Find the cells and give the type of each one.
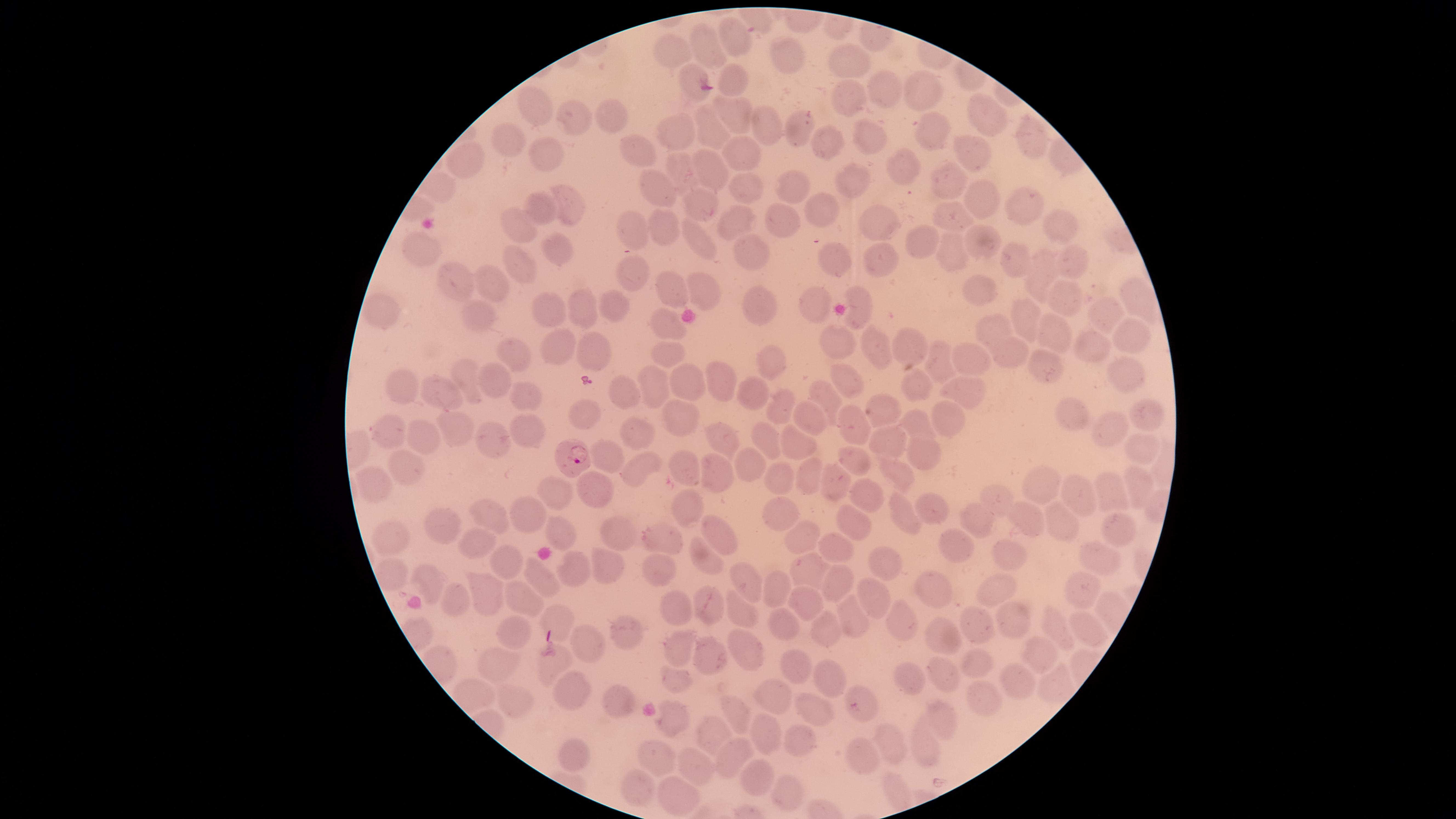
Approximate marker points as {x, y} in pixels.
Parasitized red blood cells: {575, 459}.
Uninfected red blood cells: {737, 39}, {708, 46}, {669, 52}, {783, 60}, {849, 62}, {883, 89}, {845, 95}, {918, 95}, {538, 103}, {609, 115}, {735, 116}, {983, 117}, {577, 118}, {762, 124}, {934, 127}, {795, 129}, {711, 132}, {679, 134}, {867, 137}, {828, 139}, {509, 140}, {1034, 141}, {542, 149}, {639, 151}, {967, 153}, {742, 155}, {466, 157}, {903, 164}, {712, 170}, {680, 171}, {851, 179}, {948, 183}, {793, 187}, {745, 190}, {657, 194}, {980, 196}, {567, 199}, {697, 206}, {1025, 206}, {825, 210}, {544, 211}, {951, 216}, {737, 218}, {783, 219}, {884, 220}, {633, 224}, {516, 226}, {1056, 226}, {669, 229}, {921, 237}, {701, 241}, {981, 243}, {419, 248}, {753, 250}, {954, 252}, {557, 253}, {832, 256}, {879, 259}, {1069, 259}, {1015, 260}, {518, 264}, {632, 271}, {1039, 275}, {454, 280}, {493, 282}, {665, 287}, {704, 293}, {982, 293}, {1135, 294}, {1062, 296}, {861, 301}, {615, 306}, {811, 306}, {579, 307}, {756, 308}, {1103, 310}, {385, 311}, {551, 311}, {477, 315}, {1025, 317}, {662, 324}, {992, 329}, {1049, 334}, {1131, 338}, {910, 342}, {874, 343}, {1100, 343}, {837, 344}, {560, 345}, {512, 351}, {592, 351}, {662, 352}, {1003, 352}, {940, 357}, {970, 360}, {769, 361}, {1046, 362}, {1124, 372}, {462, 375}, {723, 379}, {408, 380}, {500, 381}, {689, 383}, {656, 384}, {846, 386}, {918, 388}, {965, 391}, {758, 393}, {442, 394}, {619, 394}, {822, 394}, {521, 395}, {784, 400}, {577, 411}, {1067, 412}, {677, 413}, {815, 415}, {1145, 415}, {884, 416}, {942, 416}, {845, 419}, {917, 423}, {450, 424}, {385, 425}, {529, 425}, {633, 433}, {720, 433}, {1112, 434}, {768, 436}, {424, 437}, {493, 438}, {889, 439}, {794, 444}, {926, 447}, {1140, 447}, {609, 452}, {856, 458}, {750, 461}, {678, 462}, {638, 464}, {407, 469}, {720, 469}, {898, 473}, {807, 476}, {777, 478}, {837, 480}, {1135, 482}, {372, 484}, {596, 486}, {1043, 486}, {559, 492}, {1111, 493}, {994, 494}, {867, 496}, {1075, 498}, {686, 500}, {527, 504}, {933, 509}, {781, 512}, {495, 514}, {1026, 516}, {908, 517}, {984, 519}, {1058, 520}, {442, 521}, {849, 521}, {1116, 525}, {616, 526}, {712, 533}, {560, 535}, {653, 535}, {805, 536}, {479, 540}, {391, 544}, {835, 548}, {954, 548}, {1003, 552}, {709, 558}, {1104, 558}, {504, 559}, {888, 562}, {600, 564}, {569, 568}, {811, 569}, {658, 571}, {391, 575}, {431, 578}, {745, 580}, {542, 581}, {835, 583}, {775, 589}, {991, 590}, {488, 591}, {929, 591}, {1081, 592}, {873, 595}, {516, 598}, {459, 603}, {802, 604}, {671, 605}, {698, 605}, {557, 614}, {735, 614}, {853, 620}, {900, 620}, {975, 620}, {1020, 621}, {1079, 625}, {789, 626}, {1058, 628}, {826, 631}, {626, 632}, {519, 634}, {936, 634}, {584, 644}, {678, 645}, {746, 651}, {712, 652}, {1036, 653}, {495, 660}, {977, 663}, {551, 666}, {797, 669}, {944, 674}, {676, 680}, {823, 680}, {913, 680}, {1023, 682}, {571, 684}, {619, 695}, {979, 697}, {769, 698}, {513, 699}, {735, 705}, {863, 707}, {812, 709}, {940, 713}, {677, 718}, {713, 726}, {767, 729}, {794, 741}, {894, 743}, {917, 747}, {570, 752}, {860, 756}, {663, 757}, {689, 760}, {725, 760}, {759, 774}, {642, 788}, {895, 791}, {786, 793}, {676, 795}.
No white blood cells identified.

Image is 1456×819 pixels. Giemsa-stained preparation. Thin blood smear. One field of view of the specimen. Species: Plasmodium falciparum. The visible region is circular. Photographed with a smartphone camera through the microscope eyepiece.